Locate every P. falciparum parasite and give its life-cycle stage, and locate every leukocyte and any debris.
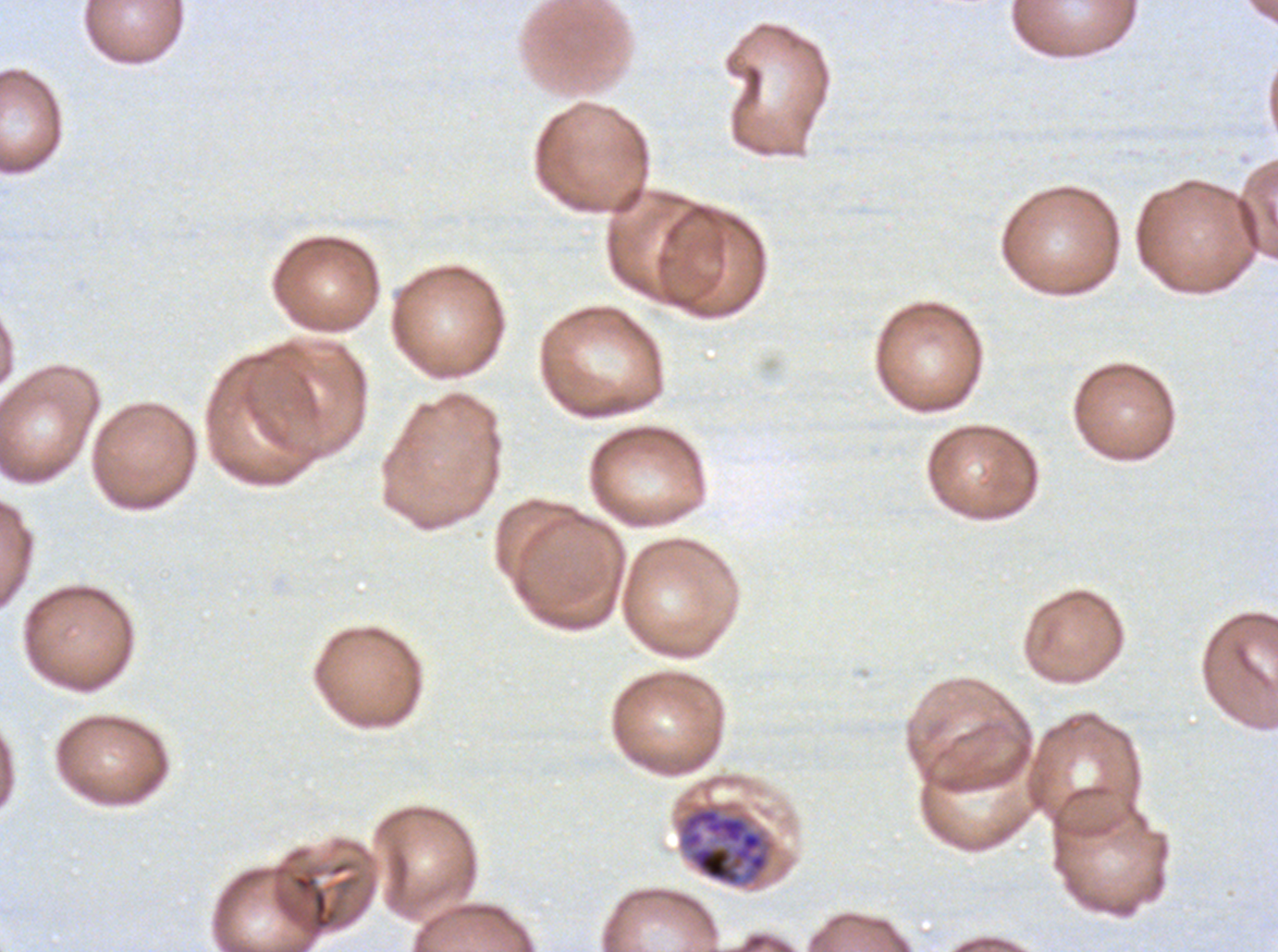
Approximate bounding boxes as {x1, y1, x2, y2} in pixels.
Late schizonts: {678, 803, 774, 887}.
Debris: {292, 873, 338, 930}.
No rings, late-ring/early-trophozoite forms, mid trophozoites, late trophozoites, early schizonts, segmenters, gametocytes, or leukocytes observed.

preparation = thin blood smear
specimen = ex-vivo P. falciparum culture from a patient in The Gambia, grown for 24 to 48 hours
field of view = sub-image separated from a larger composite
stain = Giemsa
image size = 1278×952 pixels